Point out each Plasmodium parasite.
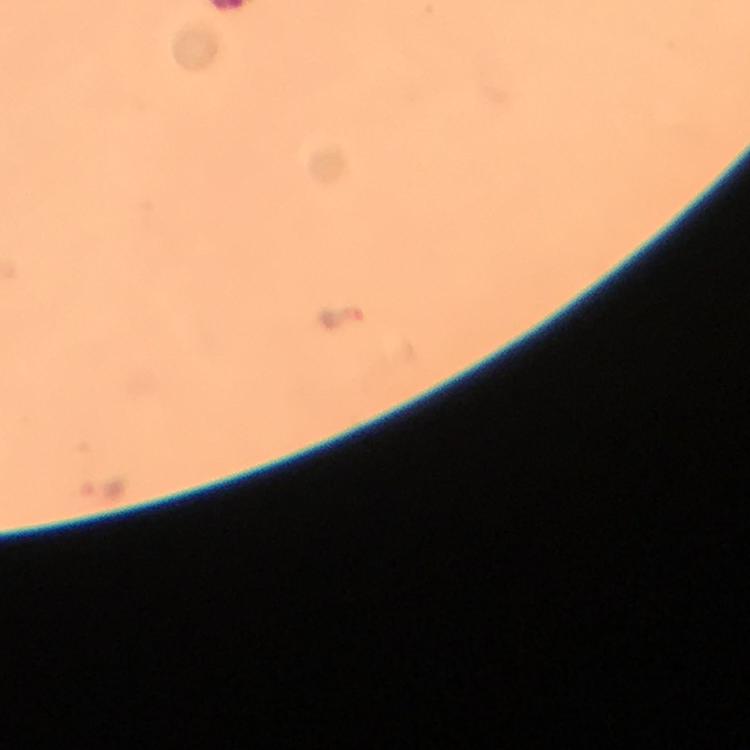
Approximate centers as [x, y] in pixels.
Plasmodium parasites: [342, 317].

Summary:
  - Capture: smartphone mounted on the microscope
  - Context: from a malaria diagnostic workup
  - Image size: 750×750 pixels
  - Magnification: 100x
  - Immersion oil: applied
  - Cropped from: a single field of view
  - Stain: Giemsa
  - Preparation: thick blood film